Identify the cell.
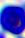
A leukocyte.

Photomicrograph. Captured at 400x magnification.